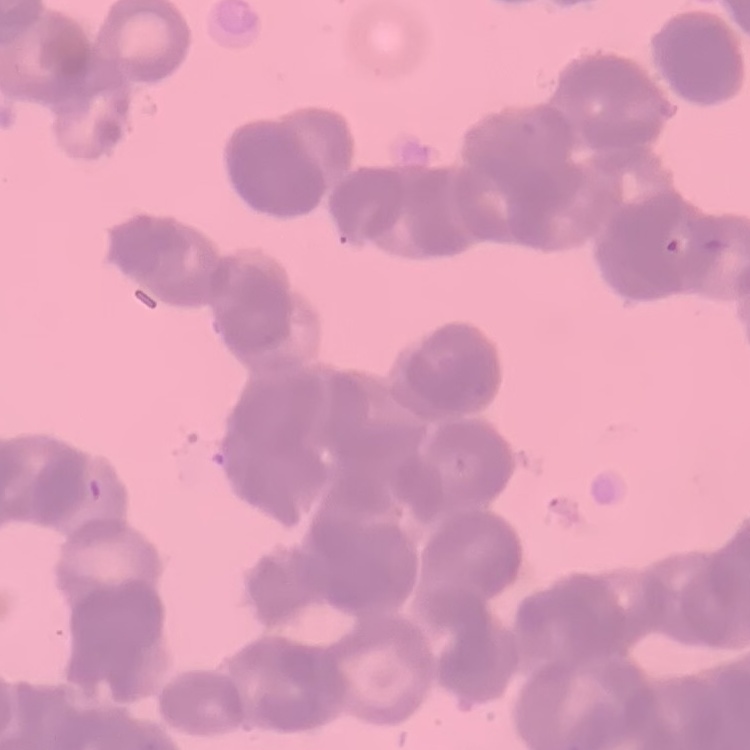

Summary:
  - Erythrocyte morphology: rouleaux formation
  - Image type: square crop of a larger photomicrograph
  - Preparation: thin blood film
  - Stain: Field's or Giemsa